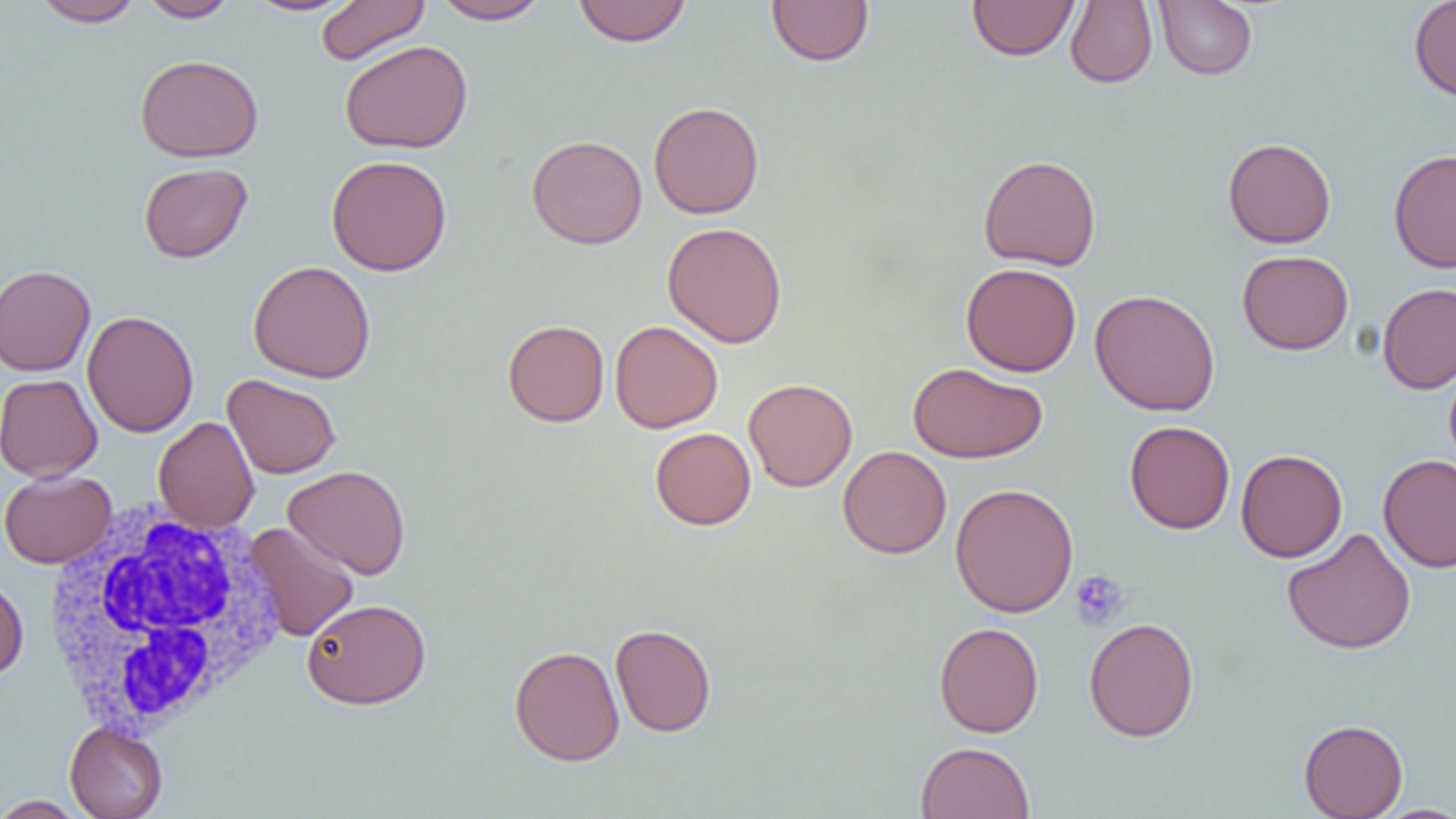
{
  "slide_level_diagnosis": "no evidence of blood parasites",
  "preparation": "thin blood smear",
  "magnification": "1000x",
  "image_size": "1456×819 pixels",
  "uninfected_red_blood_cell_locations": "approximate bounding boxes as (x1,y1)-(x2,y2) corner pairs in pixels: (33,0)-(144,27), (138,0)-(239,23), (242,0)-(362,16), (315,0)-(430,66), (432,0)-(550,24), (767,0)-(874,67), (967,0)-(1079,61), (1065,0)-(1157,88), (1409,0)-(1456,101), (573,1)-(692,47), (1154,1)-(1257,80), (340,39)-(473,154), (135,54)-(264,162), (648,101)-(764,219), (526,134)-(647,249), (1222,137)-(1336,248), (1388,149)-(1456,273), (978,154)-(1101,271), (326,155)-(452,276), (139,162)-(252,263), (662,222)-(787,347), (1237,250)-(1353,355), (248,260)-(377,383), (960,262)-(1081,376), (0,264)-(96,376), (1377,282)-(1456,394), (1090,289)-(1220,416), (82,310)-(199,438), (502,320)-(609,427), (609,320)-(723,433), (908,362)-(1048,463), (0,373)-(102,482), (223,374)-(340,479), (743,377)-(858,492), (154,417)-(259,532), (1124,420)-(1235,534), (650,427)-(756,530), (838,445)-(951,559), (1235,448)-(1347,563), (1378,455)-(1456,572), (283,465)-(410,579), (0,470)-(117,568), (950,483)-(1078,617), (243,522)-(359,642), (1282,527)-(1416,654), (0,577)-(29,680), (303,599)-(431,708), (1084,617)-(1200,742), (934,622)-(1043,738), (610,623)-(716,736), (509,645)-(624,765), (1298,718)-(1408,818), (65,722)-(168,819), (915,741)-(1035,819), (0,795)-(87,818), (1372,804)-(1456,818)",
  "white_blood_cell_locations": "approximate bounding boxes as (x1,y1)-(x2,y2) corner pairs in pixels: (41,503)-(289,735)",
  "platelet_locations": "approximate bounding boxes as (x1,y1)-(x2,y2) corner pairs in pixels: (1071,570)-(1130,630)",
  "modality": "light microscopy",
  "field_of_view": "one of a larger specimen"
}